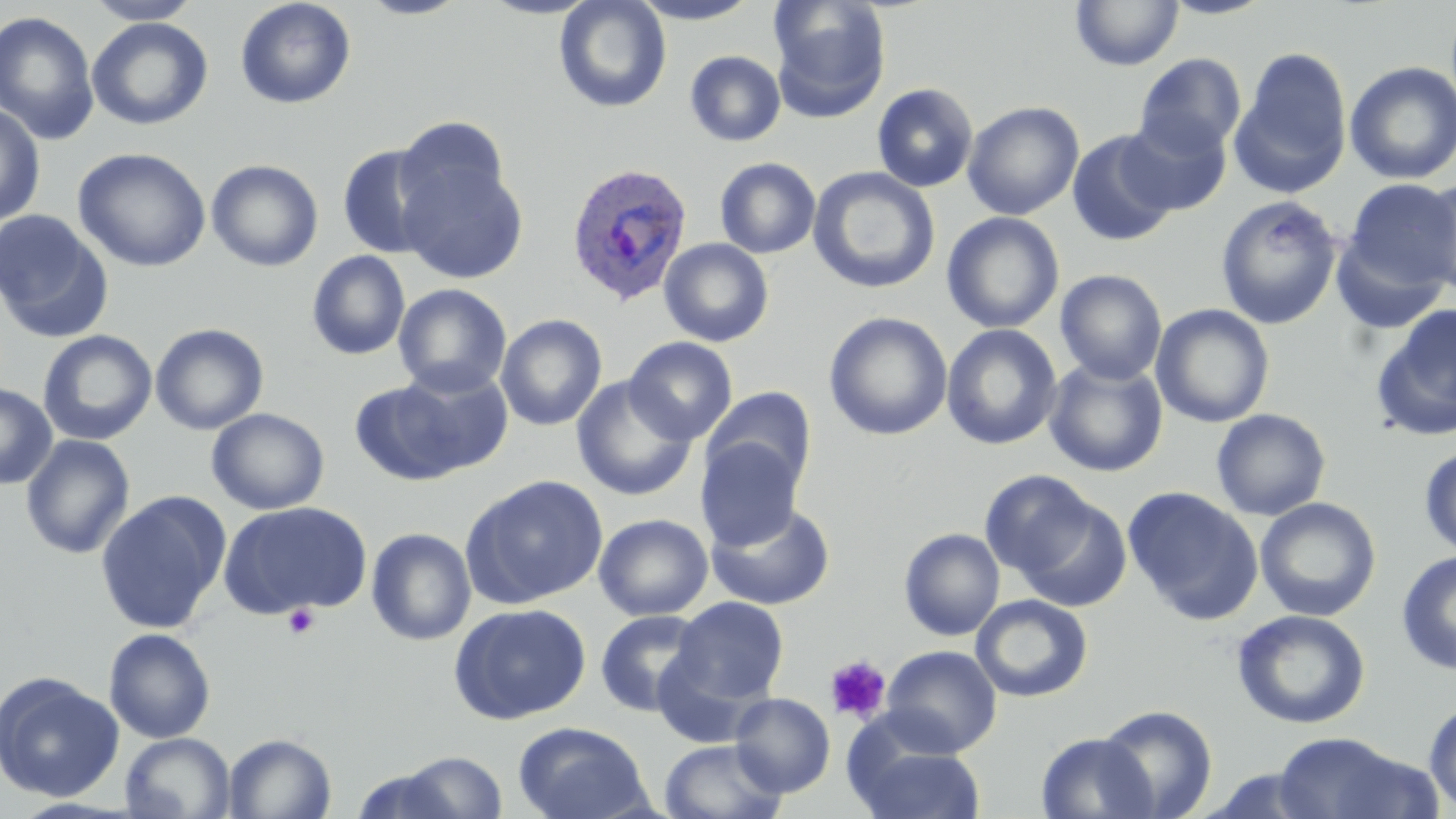

slide_level_diagnosis: Plasmodium ovale
magnification: 1000x
preparation: thin blood smear
image_size: 1456×819 pixels
modality: light microscopy
plasmodium_ovale_infected_red_blood_cell_locations: 'approximate bounding boxes as (x1, y1, x2, y2) in pixels: (565, 162, 693, 307)'
field_of_view: single
uninfected_red_blood_cell_locations: 'approximate bounding boxes as (x1, y1, x2, y2) in pixels: (83, 0, 203, 25), (235, 0, 356, 109), (355, 0, 471, 20), (479, 0, 601, 19), (554, 0, 672, 113), (628, 0, 764, 24), (768, 0, 891, 120), (1159, 0, 1277, 19), (1071, 1, 1184, 71), (0, 10, 100, 145), (87, 17, 213, 130), (1233, 47, 1353, 196), (685, 50, 786, 146), (1134, 52, 1247, 158), (1344, 61, 1456, 185), (872, 83, 978, 192), (962, 101, 1085, 220), (0, 103, 46, 227), (395, 116, 510, 218), (1118, 116, 1232, 217), (1066, 129, 1181, 248), (335, 143, 445, 260), (73, 147, 211, 272), (398, 153, 529, 284), (715, 157, 821, 259), (206, 160, 324, 272), (808, 167, 941, 294), (1419, 177, 1456, 296), (1344, 179, 1456, 292), (1216, 195, 1342, 329), (0, 210, 113, 343), (941, 212, 1065, 334), (1330, 229, 1452, 335), (659, 238, 774, 347), (306, 250, 411, 361), (1055, 269, 1167, 385), (393, 283, 512, 397), (1369, 303, 1456, 443), (1152, 304, 1275, 427), (823, 311, 953, 441), (496, 314, 607, 431), (150, 323, 269, 435), (941, 323, 1062, 451), (37, 330, 157, 445), (624, 336, 738, 445), (1044, 358, 1168, 478), (391, 364, 513, 476), (571, 377, 698, 500), (349, 379, 468, 486), (0, 382, 57, 489), (702, 386, 817, 494), (206, 408, 330, 515), (1211, 408, 1331, 520), (20, 434, 136, 560), (696, 437, 805, 551), (1418, 444, 1456, 561), (979, 469, 1099, 581), (461, 474, 609, 607), (1123, 486, 1264, 624), (94, 490, 232, 635), (1011, 492, 1134, 613), (1254, 497, 1382, 622), (218, 501, 373, 619), (705, 501, 836, 611), (593, 513, 713, 621), (366, 527, 477, 646), (899, 527, 1005, 642), (1396, 551, 1456, 674), (971, 594, 1093, 703), (670, 597, 789, 707), (449, 603, 592, 725), (1232, 608, 1370, 729), (594, 610, 710, 717), (103, 627, 216, 743), (880, 645, 1002, 757), (0, 671, 123, 803), (730, 693, 835, 797), (1424, 698, 1456, 813), (1095, 704, 1219, 819), (512, 721, 653, 819), (1035, 731, 1158, 818), (120, 732, 236, 819), (1270, 732, 1435, 819), (223, 733, 337, 819), (658, 738, 789, 819), (849, 740, 988, 819), (391, 750, 510, 818), (1199, 767, 1330, 818)'
stain: May-Grünwald-Giemsa
platelet_locations: 'approximate bounding boxes as (x1, y1, x2, y2) in pixels: (283, 605, 320, 639), (825, 655, 892, 724)'